Outline each Trypanosoma brucei.
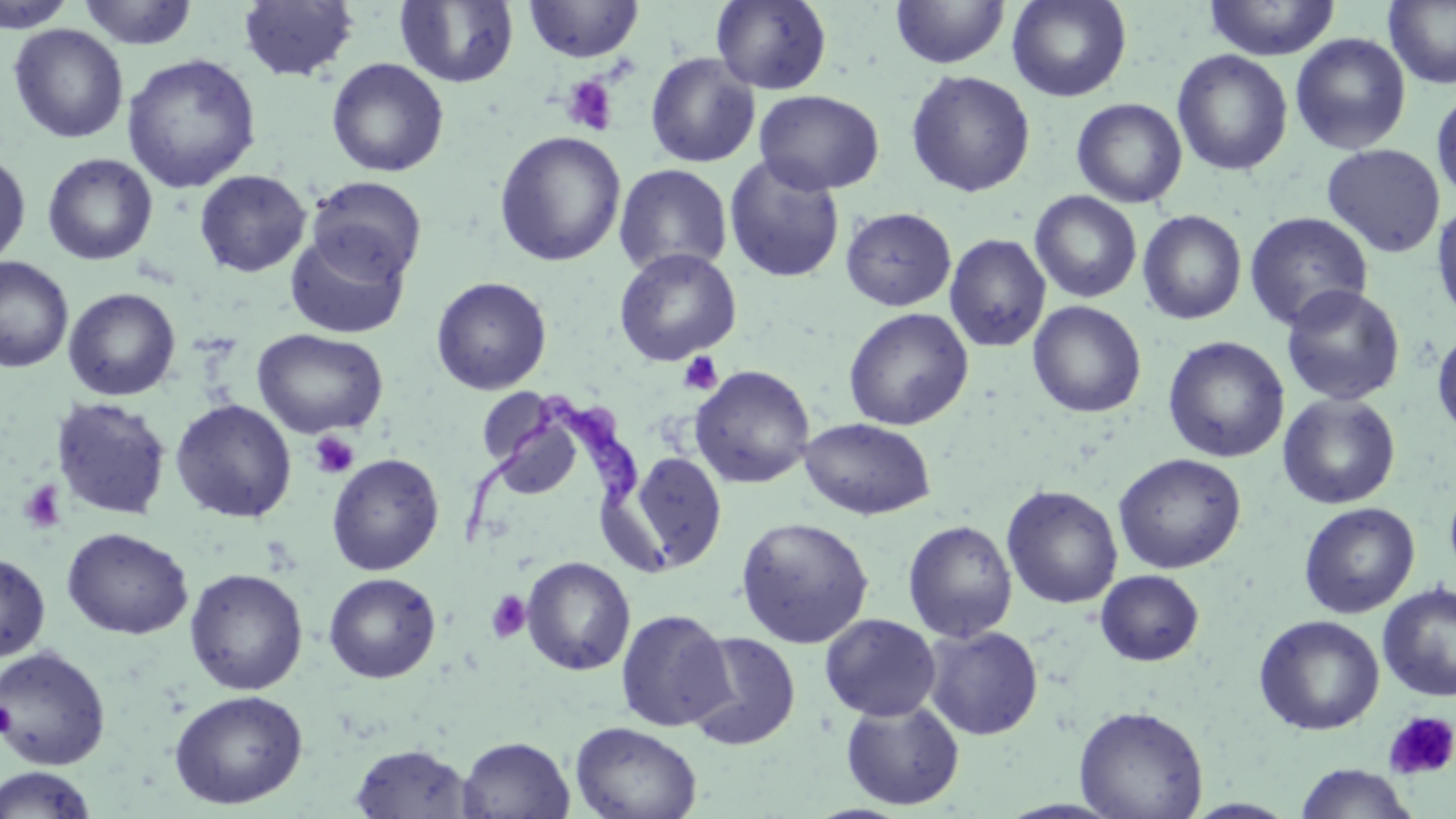
Approximate bounding boxes as named x1/y1/x2/y2 corners in pixels.
Trypanosoma brucei: (x1=456, y1=400, x2=638, y2=545).

Summary:
  - Platelet locations: (x1=561, y1=74, x2=619, y2=136), (x1=678, y1=351, x2=724, y2=396), (x1=309, y1=431, x2=360, y2=479), (x1=18, y1=480, x2=66, y2=533), (x1=484, y1=590, x2=532, y2=644), (x1=0, y1=699, x2=15, y2=739), (x1=1384, y1=710, x2=1456, y2=780)
  - Uninfected red blood cell locations: (x1=0, y1=0, x2=79, y2=32), (x1=237, y1=0, x2=359, y2=82), (x1=395, y1=0, x2=519, y2=88), (x1=523, y1=0, x2=643, y2=62), (x1=710, y1=0, x2=832, y2=94), (x1=889, y1=0, x2=1010, y2=69), (x1=1007, y1=0, x2=1131, y2=102), (x1=1203, y1=0, x2=1341, y2=60), (x1=76, y1=1, x2=201, y2=50), (x1=1384, y1=1, x2=1456, y2=89), (x1=8, y1=24, x2=129, y2=144), (x1=1290, y1=33, x2=1412, y2=155), (x1=1172, y1=49, x2=1293, y2=176), (x1=645, y1=52, x2=760, y2=168), (x1=121, y1=53, x2=262, y2=194), (x1=326, y1=58, x2=449, y2=177), (x1=905, y1=69, x2=1036, y2=198), (x1=1431, y1=88, x2=1456, y2=204), (x1=753, y1=89, x2=884, y2=195), (x1=1071, y1=98, x2=1187, y2=208), (x1=494, y1=131, x2=627, y2=267), (x1=1321, y1=143, x2=1446, y2=258), (x1=0, y1=148, x2=31, y2=269), (x1=42, y1=153, x2=158, y2=266), (x1=723, y1=155, x2=846, y2=283), (x1=613, y1=164, x2=733, y2=278), (x1=194, y1=169, x2=311, y2=277), (x1=307, y1=176, x2=427, y2=282), (x1=1030, y1=190, x2=1143, y2=303), (x1=1431, y1=199, x2=1456, y2=326), (x1=841, y1=207, x2=956, y2=311), (x1=1138, y1=210, x2=1247, y2=324), (x1=1244, y1=211, x2=1373, y2=330), (x1=283, y1=228, x2=412, y2=340), (x1=944, y1=233, x2=1051, y2=352), (x1=613, y1=247, x2=741, y2=366), (x1=0, y1=257, x2=73, y2=373), (x1=430, y1=276, x2=552, y2=395), (x1=1280, y1=285, x2=1406, y2=405), (x1=63, y1=287, x2=181, y2=401), (x1=1028, y1=300, x2=1146, y2=418), (x1=843, y1=307, x2=974, y2=431), (x1=1432, y1=327, x2=1456, y2=441), (x1=252, y1=328, x2=388, y2=439), (x1=1163, y1=336, x2=1289, y2=463), (x1=690, y1=365, x2=815, y2=488), (x1=477, y1=387, x2=557, y2=468), (x1=1277, y1=393, x2=1401, y2=508), (x1=50, y1=397, x2=172, y2=520), (x1=170, y1=399, x2=297, y2=523), (x1=490, y1=415, x2=584, y2=500), (x1=799, y1=417, x2=937, y2=520), (x1=625, y1=450, x2=727, y2=573), (x1=326, y1=452, x2=445, y2=575), (x1=1113, y1=453, x2=1246, y2=574), (x1=1444, y1=474, x2=1456, y2=587), (x1=1001, y1=484, x2=1123, y2=609), (x1=1299, y1=501, x2=1420, y2=619), (x1=735, y1=516, x2=874, y2=648), (x1=903, y1=520, x2=1017, y2=643), (x1=62, y1=527, x2=193, y2=639), (x1=0, y1=552, x2=51, y2=662), (x1=521, y1=556, x2=635, y2=676), (x1=185, y1=568, x2=308, y2=695), (x1=1095, y1=570, x2=1204, y2=666), (x1=323, y1=572, x2=442, y2=684), (x1=1377, y1=583, x2=1456, y2=702), (x1=615, y1=608, x2=732, y2=732), (x1=819, y1=613, x2=941, y2=721), (x1=1254, y1=614, x2=1385, y2=735), (x1=923, y1=626, x2=1044, y2=740), (x1=685, y1=631, x2=801, y2=751), (x1=1, y1=645, x2=111, y2=770), (x1=169, y1=689, x2=308, y2=809), (x1=840, y1=698, x2=965, y2=811), (x1=1074, y1=705, x2=1208, y2=819), (x1=569, y1=722, x2=702, y2=819), (x1=457, y1=736, x2=574, y2=818), (x1=349, y1=743, x2=475, y2=818), (x1=1294, y1=763, x2=1420, y2=819), (x1=0, y1=766, x2=99, y2=819)
  - Slide-level diagnosis: Trypanosoma brucei
  - Field of view: one of a larger specimen
  - Magnification: 1000x
  - Image size: 1456×819 pixels
  - Preparation: thin blood film
  - Modality: optical microscopy
  - Stain: May-Grünwald-Giemsa